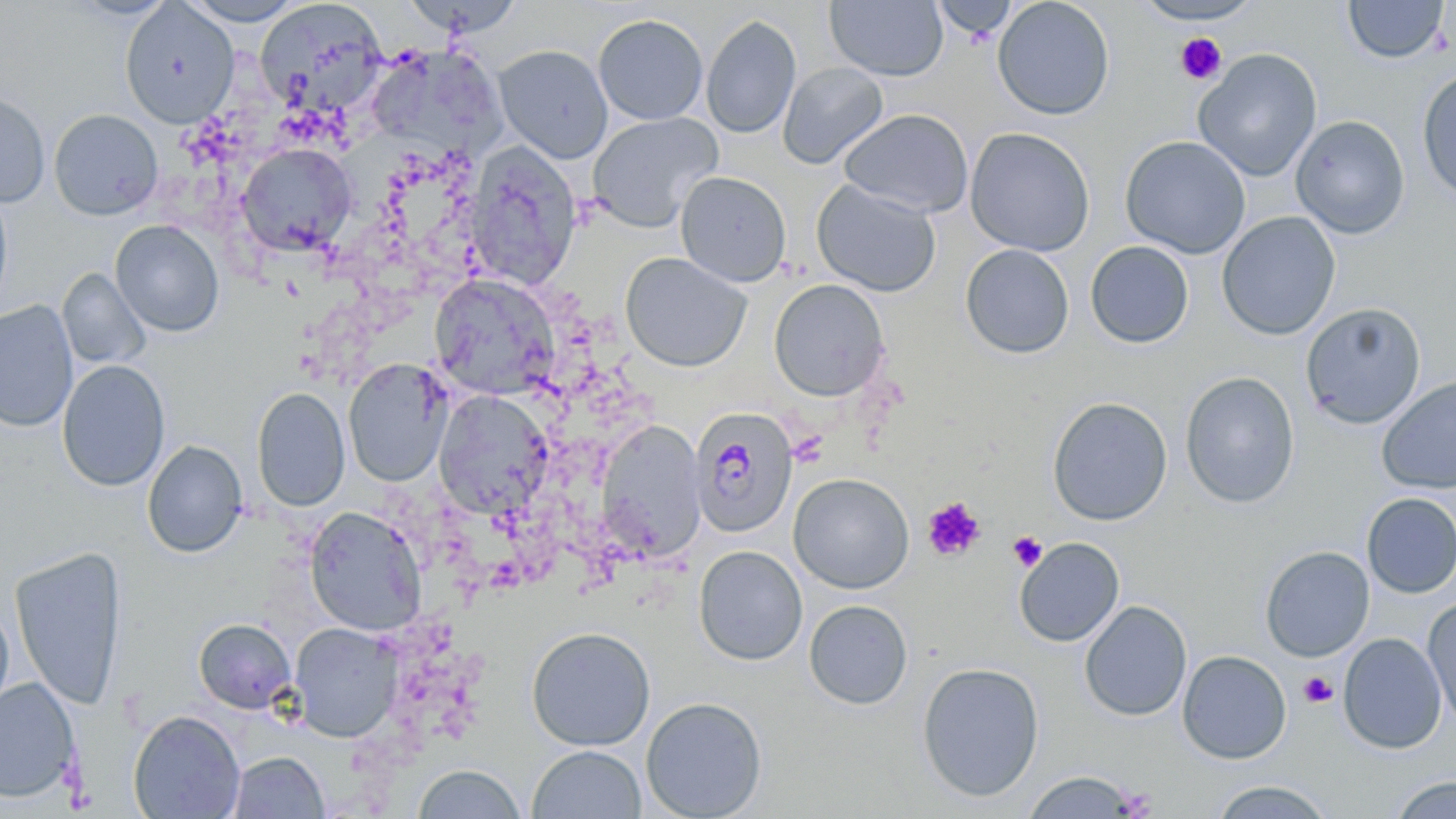

Approximate bounding boxes as (x1, y1, x2, y2) in pixels. Uninfected red blood cell locations: (66, 0, 180, 21), (179, 0, 307, 26), (931, 0, 1018, 41), (992, 0, 1115, 120), (1341, 0, 1450, 64), (255, 1, 388, 117), (824, 1, 948, 81), (1133, 1, 1264, 27), (120, 2, 239, 127), (592, 14, 709, 125), (700, 14, 801, 139), (493, 44, 614, 164), (371, 47, 513, 161), (1192, 48, 1323, 182), (777, 61, 889, 169), (1415, 66, 1456, 203), (0, 91, 50, 208), (838, 108, 974, 217), (48, 109, 164, 220), (586, 112, 724, 232), (1290, 115, 1411, 239), (964, 127, 1095, 256), (1119, 135, 1251, 259), (465, 142, 582, 290), (235, 143, 357, 257), (675, 171, 792, 287), (811, 179, 943, 298), (0, 186, 13, 311), (1216, 211, 1341, 341), (110, 220, 225, 337), (1085, 241, 1194, 348), (960, 243, 1075, 358), (620, 252, 752, 372), (57, 268, 151, 371), (429, 274, 559, 400), (769, 279, 891, 402), (0, 301, 78, 433), (1300, 302, 1426, 429), (57, 359, 171, 492), (342, 359, 453, 487), (1179, 371, 1301, 508), (1377, 375, 1456, 495), (251, 387, 350, 512), (433, 390, 555, 520), (1047, 396, 1172, 526), (596, 420, 707, 563), (142, 440, 248, 558), (788, 472, 915, 594), (1361, 492, 1456, 598), (304, 507, 427, 635), (1014, 537, 1125, 647), (693, 545, 808, 665), (1260, 546, 1375, 662), (9, 547, 128, 711), (1422, 598, 1456, 728), (804, 599, 913, 709), (1079, 600, 1192, 722), (0, 601, 14, 720), (193, 618, 297, 713), (289, 622, 404, 743), (525, 625, 656, 751), (1337, 632, 1447, 754), (1177, 650, 1292, 764), (916, 661, 1045, 802), (0, 678, 81, 803), (640, 697, 767, 818), (128, 710, 245, 819), (527, 744, 647, 819), (227, 750, 329, 818), (412, 762, 527, 819), (1022, 770, 1142, 818), (1388, 776, 1456, 819), (1209, 780, 1336, 819). Plasmodium malariae-infected red blood cell locations: (689, 405, 799, 539). Platelet locations: (1174, 33, 1228, 85), (922, 497, 986, 561), (1007, 530, 1048, 572), (1299, 672, 1338, 709), (1114, 785, 1158, 818). Slide-level diagnosis: Plasmodium malariae. 1000x magnification. May-Grünwald-Giemsa-stained preparation. Thin blood film. Image is 1456×819 pixels. Optical microscopy. Single field of view.